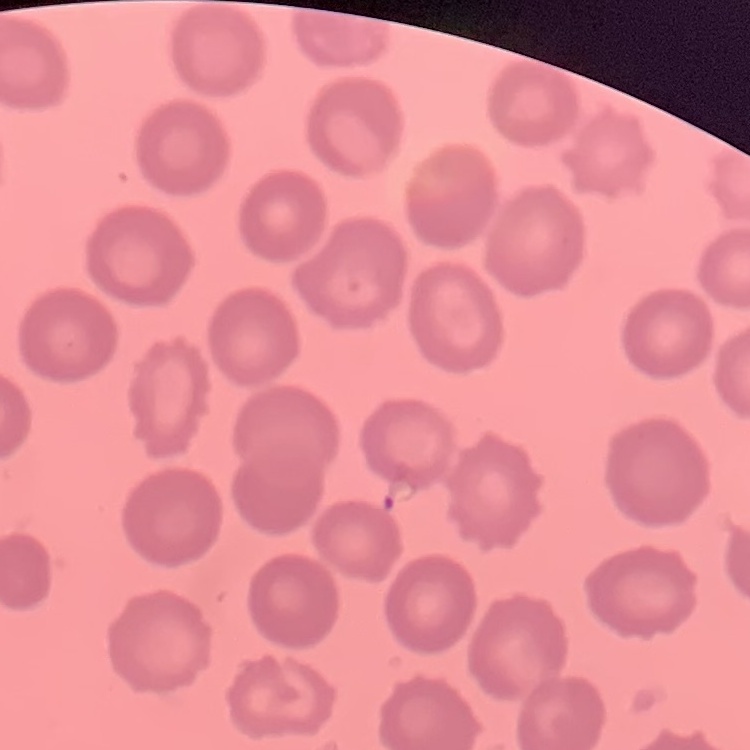
The red blood cells exhibit no rouleaux formation. Thin peripheral smear. One tile cut from a larger photomicrograph. Field's or Giemsa stain.